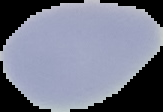 Malaria status: uninfected. From a thin blood film. Image is 163×112 pixels. Segmented cell region on a black background.